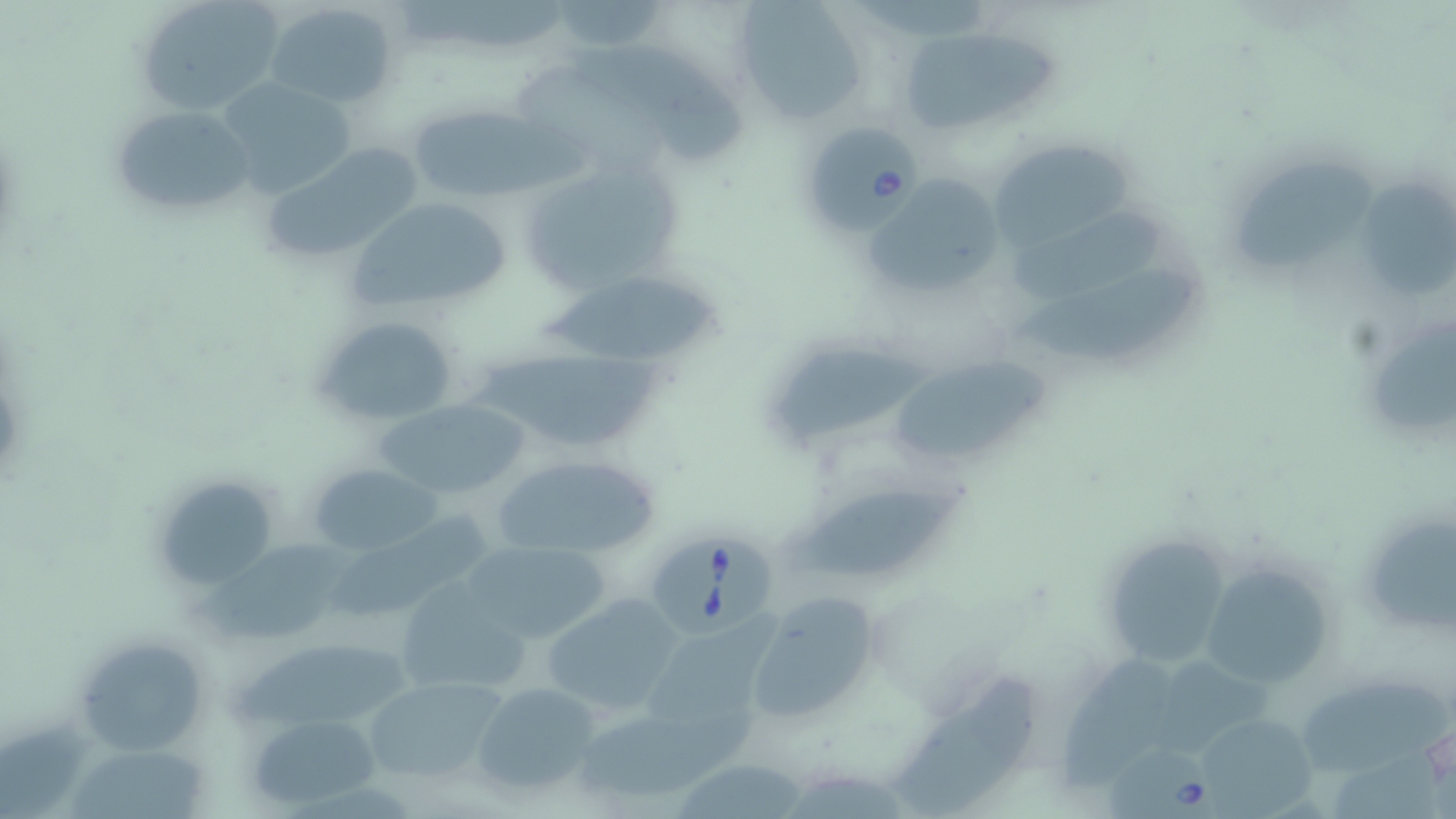
Summary:
  - Coordinate format: approximate bounding boxes as (x1, y1, x2, y2) in pixels
  - Babesia divergens-infected red blood cell locations: (800, 122, 920, 231), (650, 531, 780, 640), (1108, 746, 1220, 819)
  - Uninfected red blood cell locations: (132, 0, 285, 117), (732, 0, 871, 123), (265, 1, 401, 109), (896, 25, 1055, 136), (601, 44, 751, 166), (213, 76, 356, 199), (107, 103, 259, 219), (406, 105, 538, 203), (986, 137, 1141, 256), (261, 144, 420, 265), (1239, 153, 1374, 273), (512, 156, 690, 304), (866, 174, 1006, 303), (1362, 177, 1456, 298), (346, 196, 510, 312), (1014, 204, 1172, 300), (1019, 263, 1199, 366), (532, 277, 728, 361), (310, 314, 463, 429), (1370, 316, 1456, 425), (477, 339, 670, 448), (779, 344, 937, 453), (892, 344, 1048, 457), (377, 398, 530, 502), (491, 454, 659, 560), (308, 463, 441, 557), (148, 473, 280, 592), (796, 482, 968, 579), (1355, 501, 1456, 642), (338, 512, 489, 618), (1100, 533, 1233, 670), (189, 538, 366, 646), (461, 539, 612, 646), (1198, 558, 1336, 689), (393, 581, 531, 698), (742, 591, 887, 728), (539, 593, 684, 716), (649, 610, 784, 740), (70, 633, 210, 756), (1066, 655, 1180, 791), (359, 673, 511, 786), (894, 676, 1042, 816), (1304, 677, 1453, 771), (470, 681, 605, 801), (575, 705, 765, 807), (248, 711, 379, 810), (1190, 714, 1321, 813), (72, 747, 217, 819), (674, 763, 810, 819)
  - Slide-level diagnosis: Babesia divergens
  - Magnification: 1000x
  - Stain: May-Grünwald-Giemsa
  - Field of view: single
  - Modality: light microscopy
  - Image size: 1456×819 pixels
  - Preparation: thin blood film